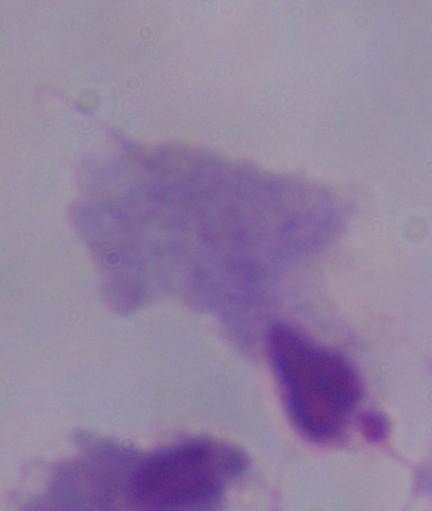
Summary:
  - Identification: trichomonad
  - Magnification: 1000x
  - Modality: micrograph